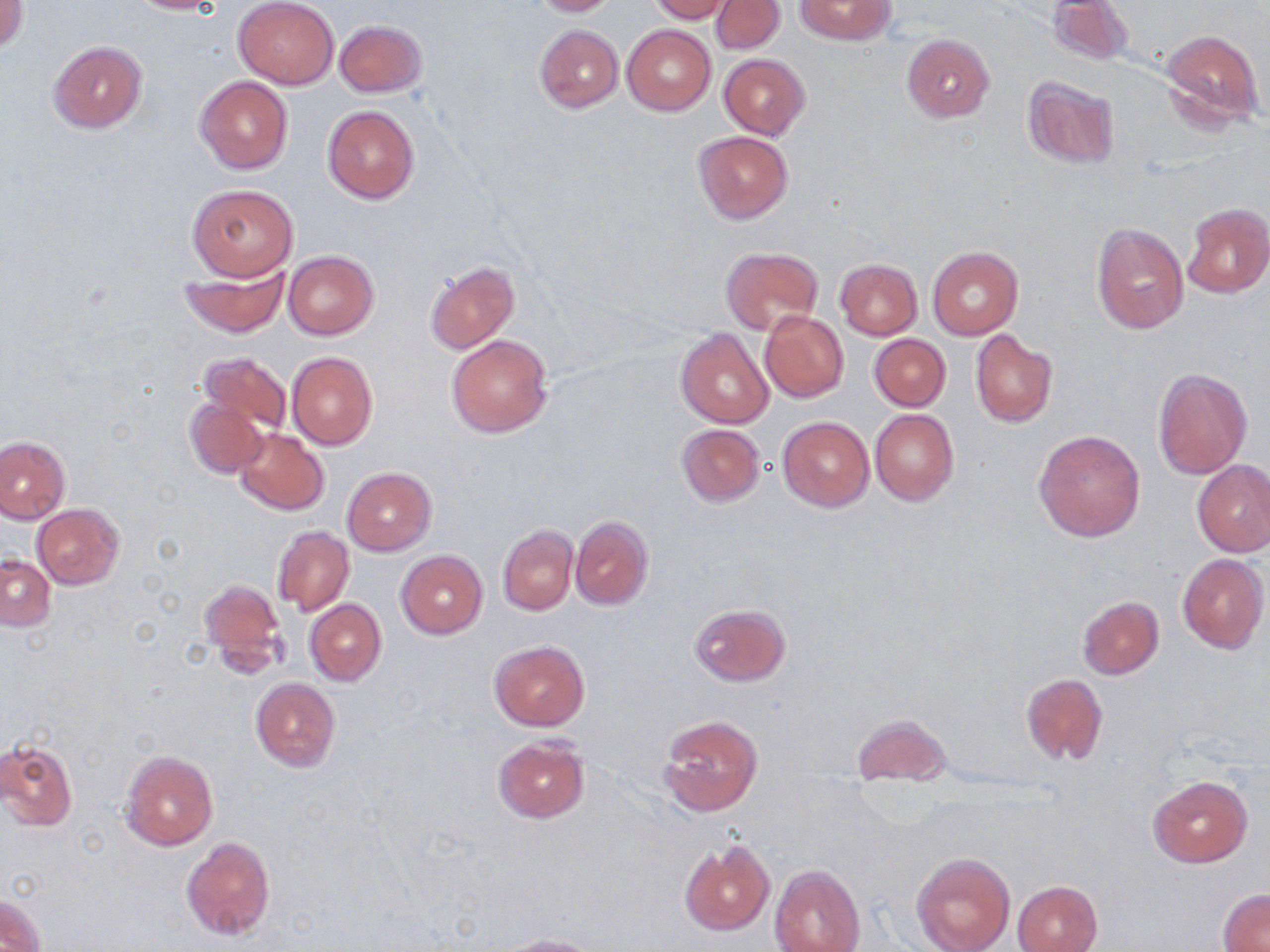

slide_level_diagnosis: no evidence of blood parasites
preparation: thin blood film
image_size: 1270×952 pixels
field_of_view: one of a larger specimen
stain: May-Grünwald-Giemsa
magnification: 1000x
uninfected_red_blood_cell_locations: 'approximate bounding boxes as (x1, y1, x2, y2) in pixels: (1, 0, 27, 52), (121, 0, 226, 14), (233, 0, 339, 87), (528, 0, 619, 16), (648, 0, 733, 23), (712, 0, 784, 53), (794, 0, 896, 44), (1045, 0, 1133, 66), (334, 19, 428, 97), (534, 24, 622, 113), (622, 24, 715, 116), (1160, 27, 1266, 132), (902, 33, 995, 122), (49, 41, 146, 134), (719, 54, 809, 140), (195, 76, 293, 174), (1022, 77, 1119, 169), (322, 105, 420, 204), (695, 130, 793, 222), (188, 182, 299, 281), (1182, 203, 1270, 297), (1091, 223, 1189, 336), (927, 245, 1023, 340), (721, 247, 822, 334), (283, 250, 378, 341), (834, 259, 922, 339), (424, 261, 518, 354), (179, 264, 289, 338), (759, 311, 848, 401), (676, 328, 774, 428), (971, 330, 1057, 428), (447, 334, 554, 437), (869, 334, 951, 411), (287, 351, 377, 450), (199, 352, 292, 437), (1152, 366, 1251, 480), (184, 397, 270, 479), (871, 409, 959, 505), (777, 416, 874, 511), (677, 424, 765, 506), (233, 428, 329, 516), (1033, 428, 1145, 542), (0, 436, 70, 522), (1193, 460, 1270, 557), (342, 467, 436, 556), (31, 503, 125, 589), (570, 515, 654, 610), (498, 526, 578, 615), (273, 527, 354, 616), (395, 550, 487, 639), (1177, 553, 1268, 652), (1, 556, 55, 631), (200, 579, 287, 673), (1077, 596, 1163, 679), (305, 599, 386, 686), (689, 603, 791, 687), (489, 640, 589, 731), (1020, 673, 1108, 765), (250, 677, 340, 770), (851, 712, 952, 785), (657, 713, 763, 816), (493, 737, 588, 823), (1, 738, 78, 832), (120, 749, 218, 850), (1147, 775, 1253, 867), (181, 835, 275, 941), (678, 839, 775, 936), (910, 851, 1014, 952), (769, 864, 865, 952), (1012, 881, 1102, 952), (1218, 890, 1270, 950), (2, 893, 46, 951), (494, 934, 602, 952)'
modality: light microscopy